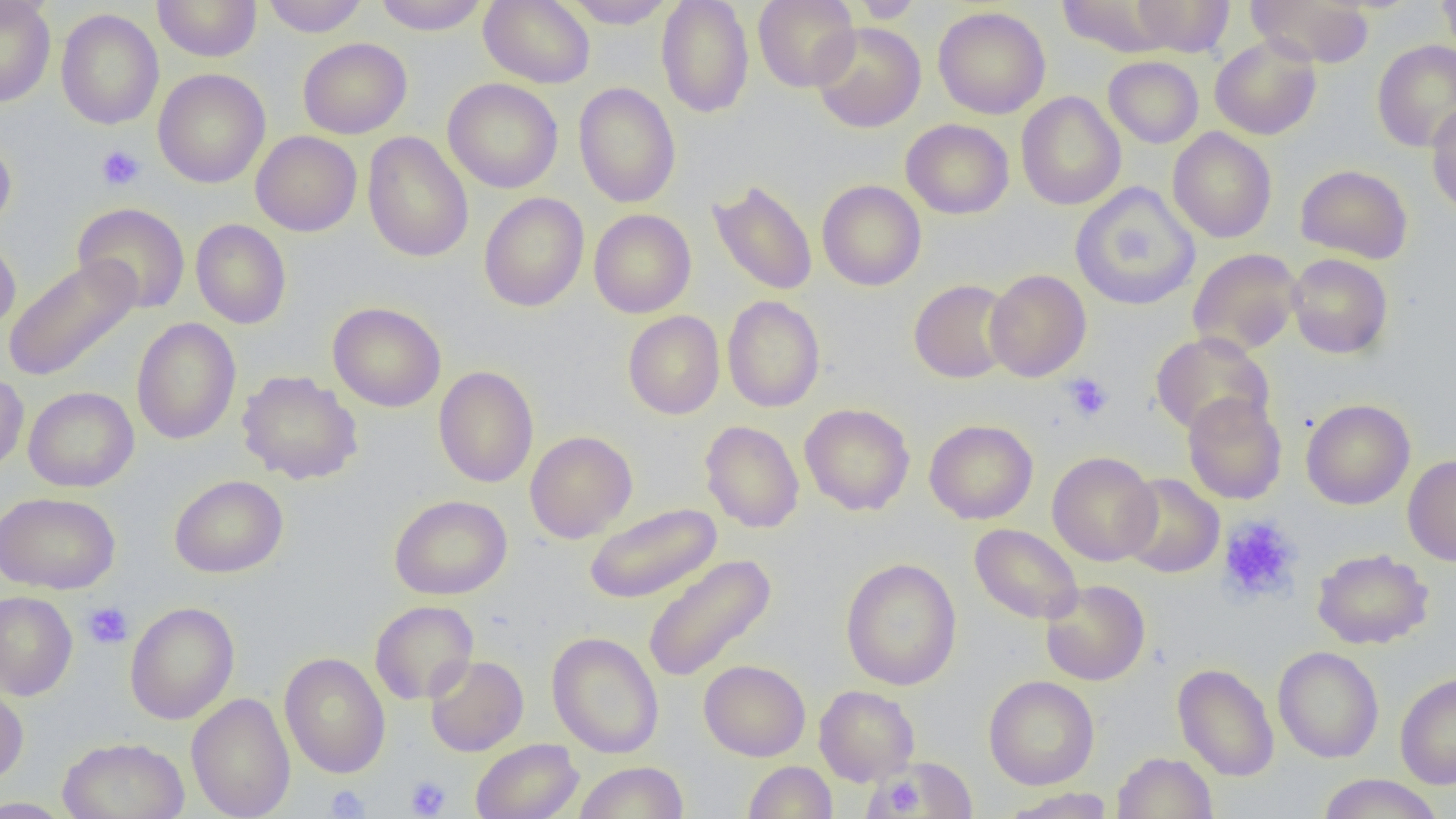

slide_level_diagnosis: no evidence of blood parasites
modality: light microscopy
image_size: 1456×819 pixels
field_of_view: single
magnification: 1000x
uninfected_red_blood_cell_locations: 'approximate bounding boxes as named x1/y1/x2/y2 corners in pixels: (x1=0, y1=0, x2=56, y2=107), (x1=153, y1=0, x2=261, y2=62), (x1=262, y1=0, x2=369, y2=36), (x1=373, y1=0, x2=490, y2=35), (x1=479, y1=0, x2=594, y2=88), (x1=563, y1=0, x2=676, y2=28), (x1=656, y1=0, x2=754, y2=118), (x1=753, y1=0, x2=860, y2=92), (x1=852, y1=0, x2=923, y2=23), (x1=1131, y1=0, x2=1234, y2=56), (x1=1248, y1=0, x2=1376, y2=67), (x1=1437, y1=0, x2=1456, y2=61), (x1=1056, y1=1, x2=1173, y2=56), (x1=933, y1=6, x2=1051, y2=119), (x1=56, y1=8, x2=164, y2=130), (x1=811, y1=22, x2=926, y2=133), (x1=1209, y1=35, x2=1322, y2=140), (x1=298, y1=37, x2=412, y2=139), (x1=1372, y1=40, x2=1456, y2=153), (x1=1103, y1=56, x2=1204, y2=148), (x1=153, y1=68, x2=270, y2=188), (x1=443, y1=78, x2=563, y2=193), (x1=573, y1=82, x2=681, y2=208), (x1=1016, y1=91, x2=1126, y2=211), (x1=1426, y1=101, x2=1456, y2=216), (x1=901, y1=118, x2=1014, y2=219), (x1=1167, y1=127, x2=1277, y2=243), (x1=251, y1=131, x2=362, y2=236), (x1=362, y1=132, x2=474, y2=263), (x1=0, y1=133, x2=17, y2=234), (x1=1295, y1=164, x2=1413, y2=264), (x1=708, y1=179, x2=818, y2=296), (x1=817, y1=180, x2=926, y2=291), (x1=1071, y1=182, x2=1200, y2=311), (x1=478, y1=193, x2=589, y2=312), (x1=73, y1=202, x2=191, y2=313), (x1=589, y1=209, x2=696, y2=318), (x1=190, y1=219, x2=292, y2=329), (x1=0, y1=234, x2=20, y2=337), (x1=1188, y1=248, x2=1304, y2=356), (x1=1287, y1=253, x2=1393, y2=359), (x1=4, y1=256, x2=142, y2=382), (x1=984, y1=269, x2=1091, y2=382), (x1=909, y1=279, x2=1015, y2=383), (x1=722, y1=295, x2=825, y2=412), (x1=328, y1=301, x2=446, y2=412), (x1=623, y1=311, x2=725, y2=419), (x1=131, y1=317, x2=241, y2=444), (x1=1150, y1=331, x2=1274, y2=438), (x1=433, y1=366, x2=539, y2=488), (x1=237, y1=370, x2=363, y2=485), (x1=0, y1=371, x2=29, y2=476), (x1=24, y1=386, x2=139, y2=492), (x1=1182, y1=392, x2=1287, y2=505), (x1=1301, y1=398, x2=1415, y2=510), (x1=799, y1=403, x2=915, y2=515), (x1=924, y1=419, x2=1038, y2=524), (x1=700, y1=420, x2=804, y2=533), (x1=525, y1=430, x2=637, y2=543), (x1=1047, y1=451, x2=1161, y2=566), (x1=1402, y1=455, x2=1456, y2=566), (x1=1119, y1=473, x2=1224, y2=577), (x1=169, y1=474, x2=289, y2=578), (x1=0, y1=491, x2=119, y2=594), (x1=389, y1=495, x2=512, y2=600), (x1=584, y1=503, x2=722, y2=604), (x1=970, y1=523, x2=1083, y2=624), (x1=1312, y1=547, x2=1433, y2=649), (x1=642, y1=554, x2=776, y2=683), (x1=841, y1=557, x2=961, y2=690), (x1=1040, y1=579, x2=1150, y2=686), (x1=0, y1=591, x2=78, y2=700), (x1=370, y1=600, x2=478, y2=705), (x1=124, y1=601, x2=239, y2=725), (x1=547, y1=631, x2=664, y2=759), (x1=1272, y1=646, x2=1384, y2=763), (x1=279, y1=652, x2=391, y2=778), (x1=424, y1=655, x2=528, y2=756), (x1=699, y1=659, x2=810, y2=761), (x1=1173, y1=663, x2=1279, y2=781), (x1=1395, y1=671, x2=1456, y2=789), (x1=984, y1=674, x2=1099, y2=790), (x1=0, y1=681, x2=29, y2=786), (x1=814, y1=685, x2=919, y2=786), (x1=186, y1=692, x2=296, y2=819), (x1=58, y1=737, x2=190, y2=819), (x1=470, y1=739, x2=583, y2=819), (x1=1112, y1=751, x2=1218, y2=819), (x1=883, y1=757, x2=977, y2=817), (x1=573, y1=761, x2=688, y2=819), (x1=743, y1=761, x2=837, y2=818), (x1=1317, y1=774, x2=1444, y2=818), (x1=1000, y1=788, x2=1114, y2=818), (x1=0, y1=796, x2=74, y2=818)'
preparation: thin blood smear
platelet_locations: 'approximate bounding boxes as named x1/y1/x2/y2 corners in pixels: (x1=96, y1=145, x2=145, y2=192), (x1=1062, y1=373, x2=1114, y2=422), (x1=1217, y1=514, x2=1303, y2=604), (x1=83, y1=601, x2=133, y2=649), (x1=405, y1=776, x2=451, y2=817), (x1=878, y1=779, x2=923, y2=816), (x1=324, y1=785, x2=369, y2=818)'